Assess this cell for malaria.
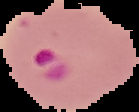
It is parasitized.

preparation = thin blood film
image size = 139×112 pixels
image type = segmented cell region with the area outside set to black